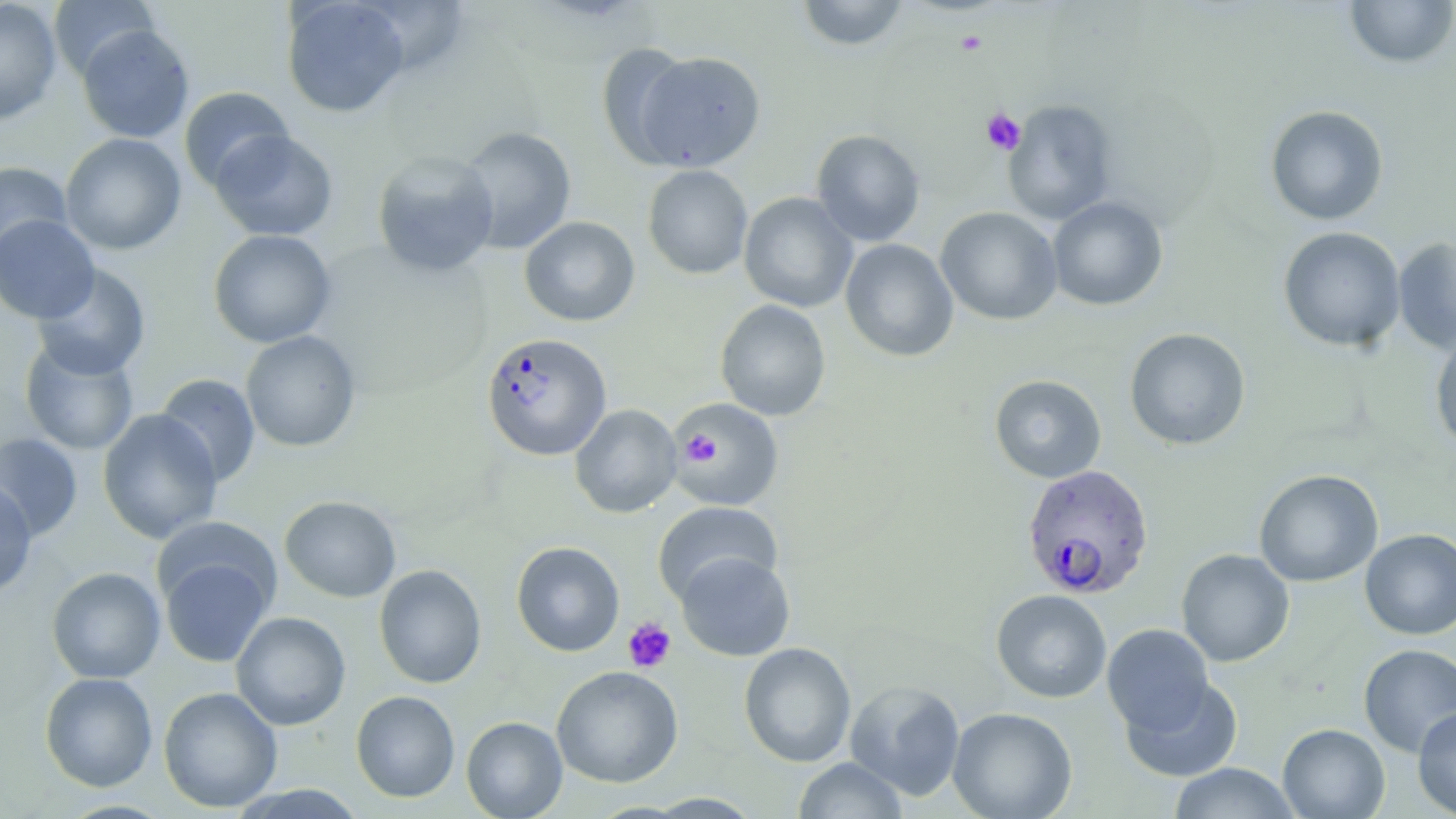
Summary:
  - Coordinate format: approximate bounding boxes as [x1, y1, x2, y2] in pixels
  - Plasmodium falciparum-infected red blood cell locations: [480, 331, 612, 461], [1021, 463, 1154, 600]
  - Platelet locations: [955, 30, 987, 56], [980, 107, 1026, 155], [680, 431, 720, 465], [622, 617, 676, 673]
  - Uninfected red blood cell locations: [0, 0, 62, 125], [48, 0, 160, 81], [281, 0, 410, 118], [795, 0, 909, 51], [1343, 0, 1456, 69], [77, 24, 195, 143], [596, 43, 696, 166], [634, 51, 766, 171], [178, 86, 294, 192], [1003, 99, 1118, 226], [1265, 105, 1389, 225], [456, 126, 577, 254], [209, 130, 338, 242], [811, 130, 925, 246], [60, 133, 186, 255], [372, 150, 500, 277], [0, 160, 72, 262], [642, 164, 753, 279], [739, 192, 858, 312], [1047, 196, 1168, 311], [935, 207, 1063, 326], [0, 215, 99, 323], [519, 216, 639, 326], [1278, 226, 1406, 352], [208, 229, 336, 348], [1393, 237, 1456, 354], [840, 238, 959, 362], [32, 263, 151, 380], [715, 299, 831, 421], [1124, 328, 1251, 450], [240, 330, 361, 452], [1430, 330, 1456, 453], [19, 338, 139, 455], [155, 373, 261, 487], [989, 374, 1107, 483], [667, 397, 785, 512], [570, 404, 682, 518], [97, 409, 223, 545], [0, 432, 83, 542], [1254, 469, 1383, 587], [0, 479, 37, 599], [279, 495, 402, 603], [653, 501, 783, 605], [152, 516, 279, 614], [1360, 528, 1456, 640], [510, 541, 625, 657], [1176, 548, 1294, 667], [158, 550, 276, 668], [675, 551, 795, 661], [373, 564, 487, 688], [46, 567, 166, 684], [991, 589, 1112, 703], [230, 611, 351, 731], [1102, 623, 1215, 734], [738, 642, 856, 767], [1358, 644, 1456, 756], [551, 665, 683, 788], [39, 671, 158, 792], [1120, 675, 1243, 782], [844, 679, 965, 801], [158, 686, 283, 813], [351, 690, 460, 803], [1412, 706, 1456, 818], [947, 707, 1077, 818], [461, 716, 567, 818], [1278, 723, 1390, 818], [793, 757, 909, 818], [1167, 762, 1301, 818], [228, 784, 367, 818], [643, 793, 763, 818]
  - Slide-level diagnosis: Plasmodium falciparum
  - Field of view: one of a larger specimen
  - Preparation: thin blood film
  - Stain: May-Grünwald-Giemsa
  - Magnification: 1000x
  - Image size: 1456×819 pixels
  - Modality: light microscopy